Look for Plasmodium parasites.
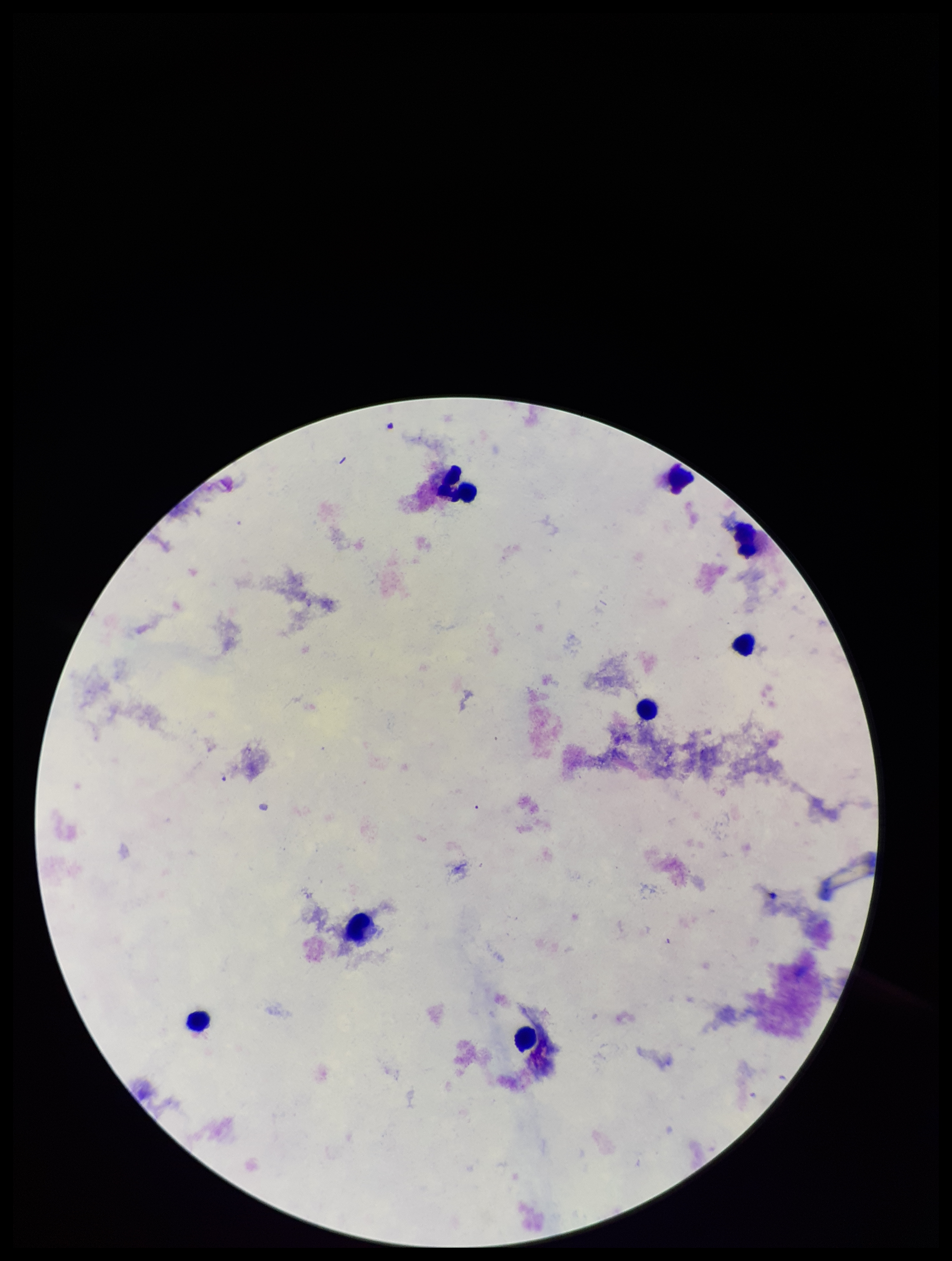
None identified.

Smartphone photograph taken through the eyepiece of a microscope. Patient malaria status: negative. Single field of view. Parasite count: 0. Image is 952×1261 pixels. Preparation: thick. Leukocyte count: 8. Stained with Giemsa.